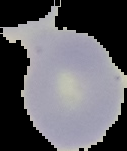

Summary:
  - Malaria status: uninfected
  - Image size: 127×151 pixels
  - Preparation: thin blood smear
  - Image type: cell region segmented out of the field of view; surrounding area masked to black